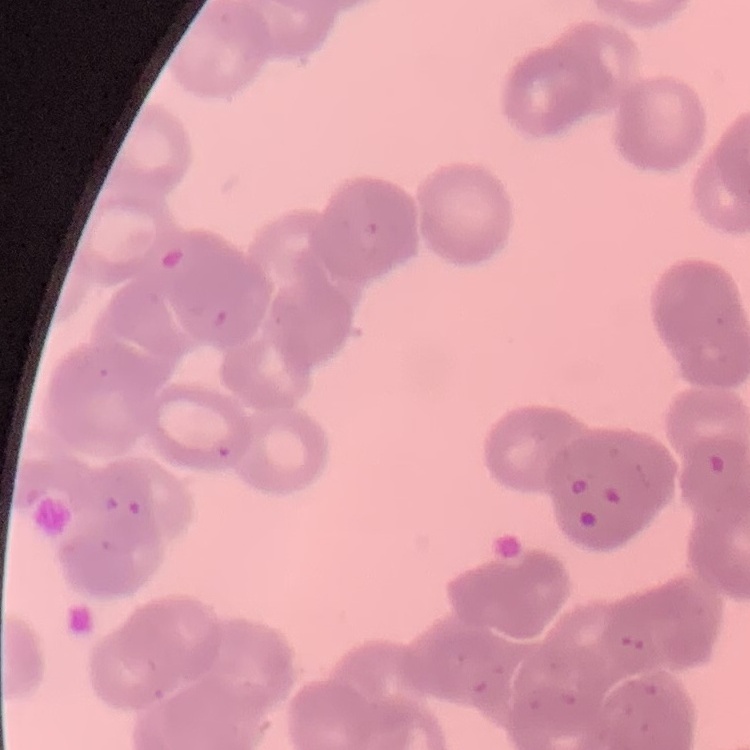

Summary:
  - Red blood cell morphology: rouleaux formation
  - Preparation: thin blood smear
  - Image type: square crop of a larger photomicrograph
  - Stain: Field's or Giemsa